Locate every Plasmodium vivax-infected red blood cell.
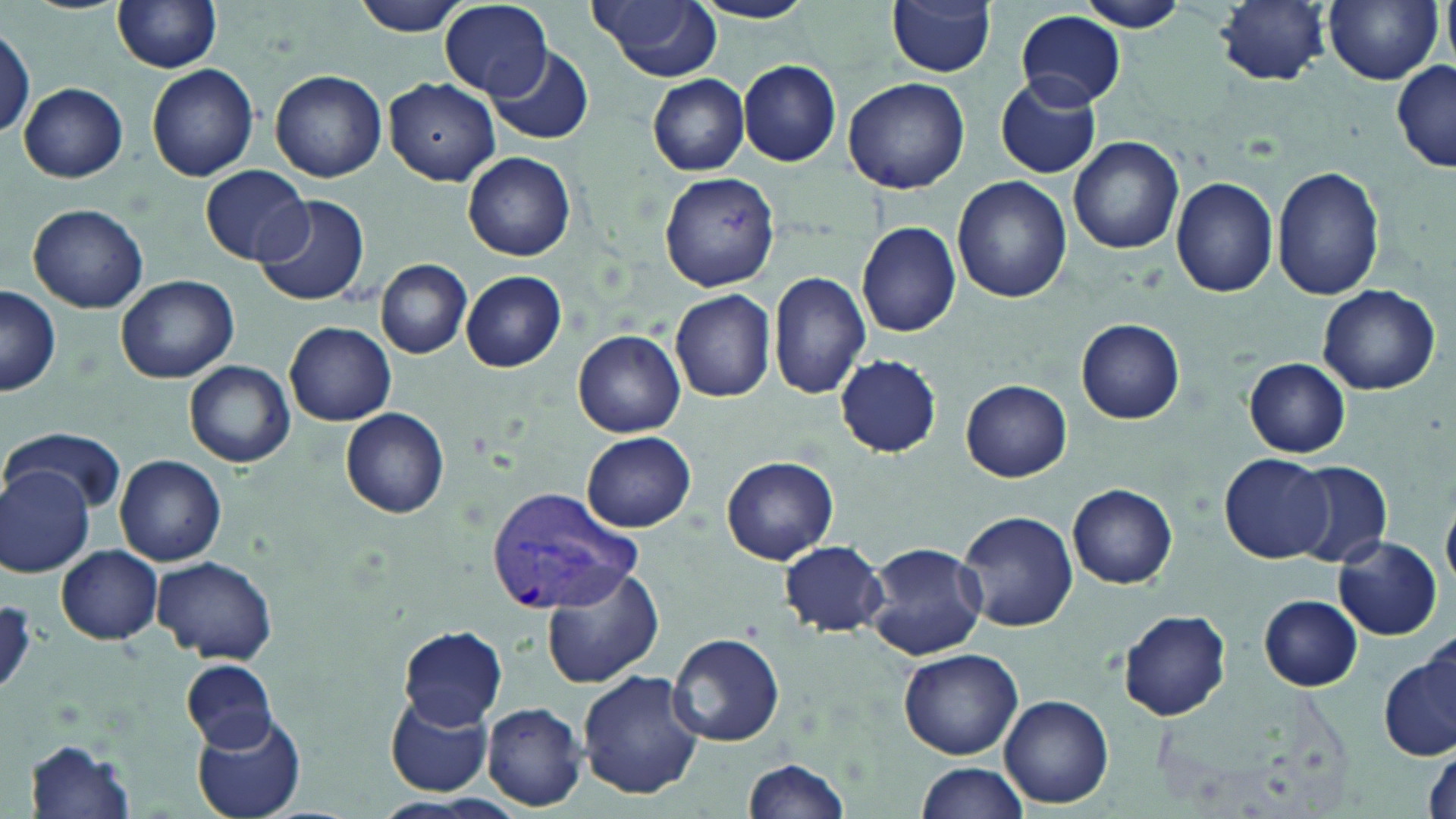
Approximate bounding boxes as (x1,y1)-(x2,y2) corner pairs in pixels.
Plasmodium vivax-infected red blood cells: (485,487)-(647,614).

{
  "slide_level_diagnosis": "Plasmodium vivax",
  "preparation": "thin blood film",
  "image_size": "1456×819 pixels",
  "uninfected_red_blood_cell_locations": "approximate bounding boxes as (x1,y1)-(x2,y2) corner pairs in pixels: (115,0)-(222,73), (352,0)-(477,37), (592,0)-(722,80), (888,0)-(997,76), (1081,0)-(1194,33), (1216,0)-(1331,84), (1323,0)-(1444,85), (689,1)-(820,25), (441,2)-(554,98), (1015,11)-(1126,109), (0,26)-(34,143), (490,45)-(593,143), (737,59)-(842,166), (1392,61)-(1455,174), (148,64)-(259,181), (269,68)-(388,182), (647,74)-(751,175), (995,75)-(1102,180), (842,76)-(971,194), (385,77)-(500,184), (19,81)-(128,182), (1068,136)-(1184,254), (463,151)-(575,261), (201,164)-(312,266), (1272,165)-(1383,301), (659,172)-(779,291), (953,175)-(1071,303), (1171,176)-(1280,298), (255,194)-(370,308), (27,203)-(149,313), (856,221)-(962,338), (375,258)-(471,359), (461,271)-(566,372), (768,271)-(871,397), (116,274)-(238,383), (1316,283)-(1440,394), (0,287)-(61,397), (670,289)-(776,403), (1076,319)-(1185,423), (284,322)-(396,425), (573,330)-(686,437), (834,355)-(943,456), (1244,358)-(1351,458), (185,360)-(295,469), (962,379)-(1072,482), (339,408)-(448,519), (6,425)-(126,513), (581,431)-(697,532), (1217,454)-(1334,563), (115,455)-(227,565), (720,455)-(837,565), (1287,462)-(1393,566), (0,468)-(94,576), (1068,483)-(1176,588), (955,508)-(1079,632), (1332,534)-(1443,639), (777,540)-(889,636), (864,540)-(989,660), (54,547)-(164,644), (153,555)-(278,665), (542,567)-(664,689), (1261,595)-(1363,691), (1118,610)-(1232,720), (400,625)-(507,729), (665,632)-(785,747), (898,647)-(1024,759), (1381,647)-(1456,763), (180,658)-(275,752), (577,670)-(704,798), (385,691)-(498,797), (999,693)-(1113,808), (479,702)-(587,812), (189,711)-(307,819), (24,738)-(136,817), (743,757)-(853,819), (915,761)-(1029,816)",
  "stain": "May-Grünwald-Giemsa",
  "modality": "light microscopy",
  "field_of_view": "one of a larger specimen",
  "magnification": "1000x"
}